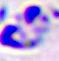

A leukocyte is seen. Captured at 400x magnification. Micrograph.